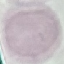
Result: no malaria parasites detected. Cell patch, automatically extracted from a larger field of view and resized to 64 × 64 pixels. Photographed with a smartphone camera at the microscope eyepiece. Thin smear of blood. Giemsa-stained preparation.